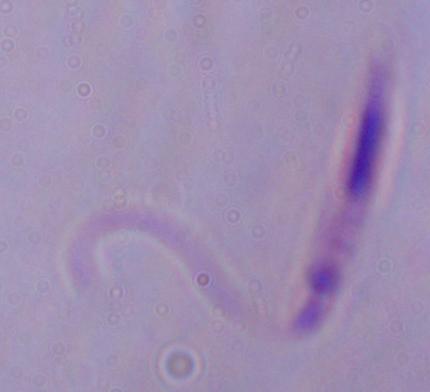

identification = Leishmania
magnification = 1000x
modality = photomicrograph